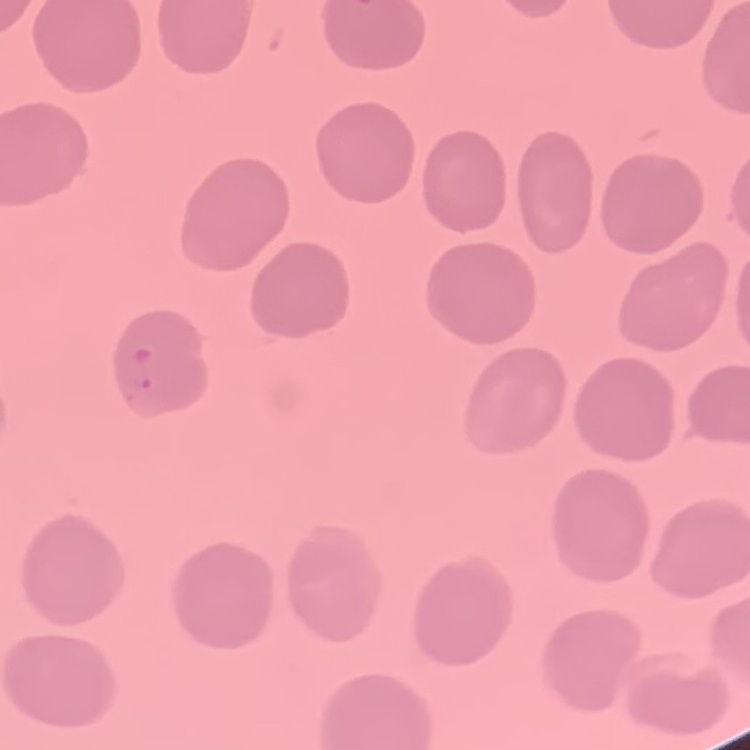
{
  "red_blood_cell_morphology": "no rouleaux formation",
  "stain": "Field's or Giemsa",
  "preparation": "thin blood film",
  "image_type": "one tile cut from a larger photomicrograph"
}